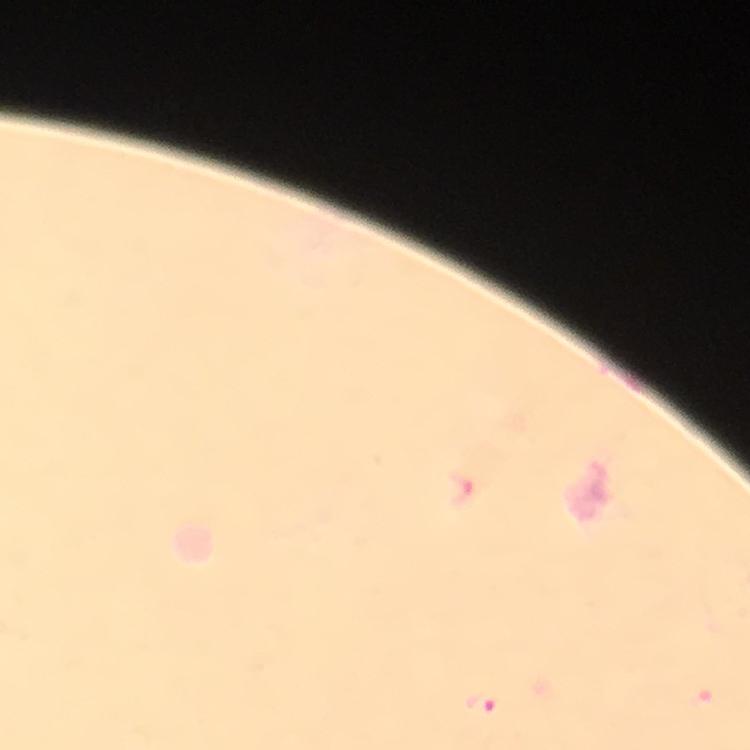

Approximate object centers, in pixels from the top-left corner.
Summary:
  - Plasmodium parasite locations: (x=481, y=702), (x=705, y=703)
  - Capture: smartphone photograph through a microscope
  - Magnification: 100x
  - Stain: Giemsa
  - Preparation: thick blood smear
  - Image size: 750×750 pixels
  - Cropped from: one field of view
  - Immersion oil: used
  - Context: from a malaria diagnostic workup